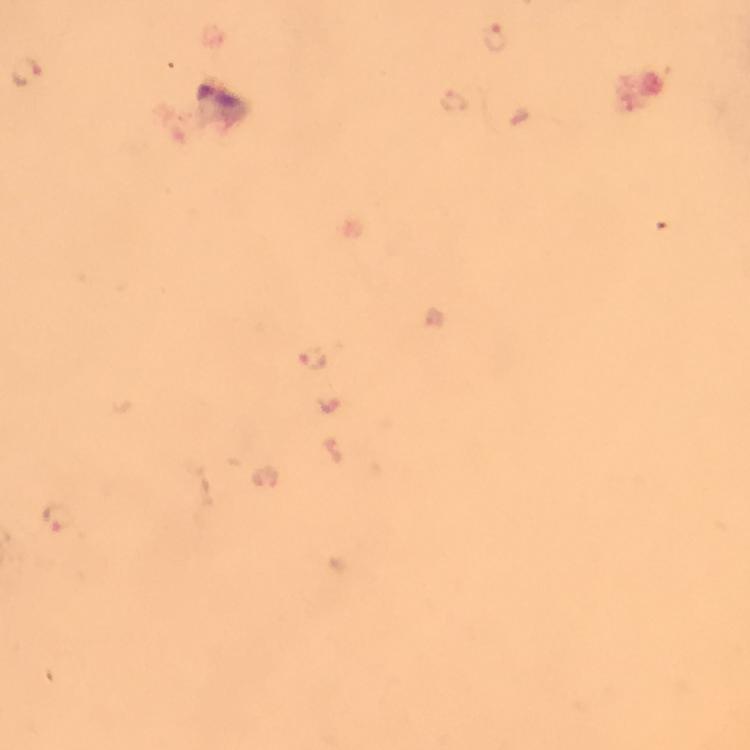

malaria parasite locations = approximate centers as {x, y} in pixels: {496, 39}, {25, 72}, {454, 102}, {313, 359}, {59, 518}
image size = 750×750 pixels
capture = smartphone mounted on the microscope
preparation = thick blood film
stain = Giemsa
context = from a malaria diagnostic workup
cropped from = one field of view
immersion oil = used
magnification = 100x